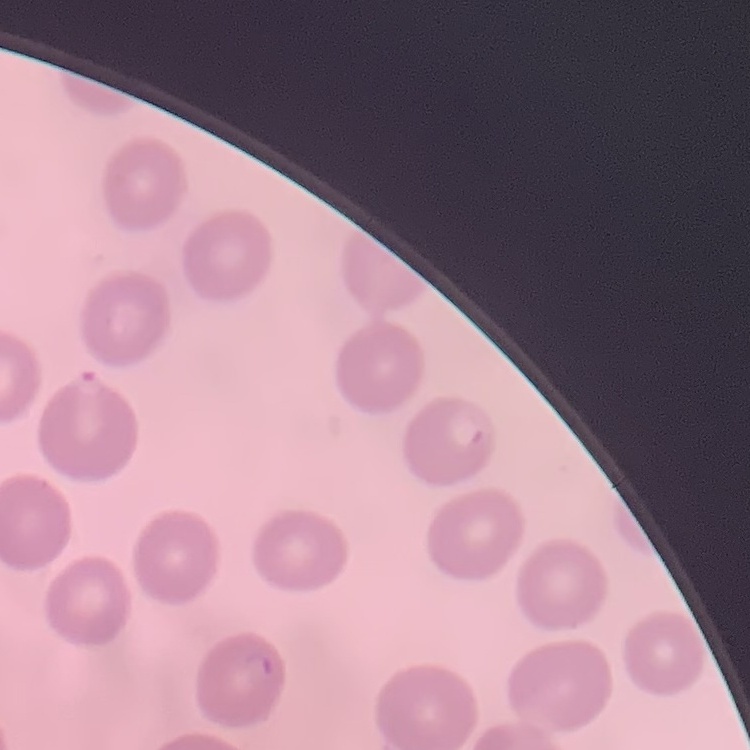 The red blood cells show no rouleaux formation. Square crop of a larger photomicrograph. Thin blood film. Field's or Giemsa stain.